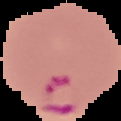

{
  "preparation": "thin blood film",
  "image_size": "121×121 pixels",
  "malaria_status": "parasitized",
  "image_type": "cell region segmented out of the field of view; surrounding area masked to black"
}